Find each parasitized red blood cell.
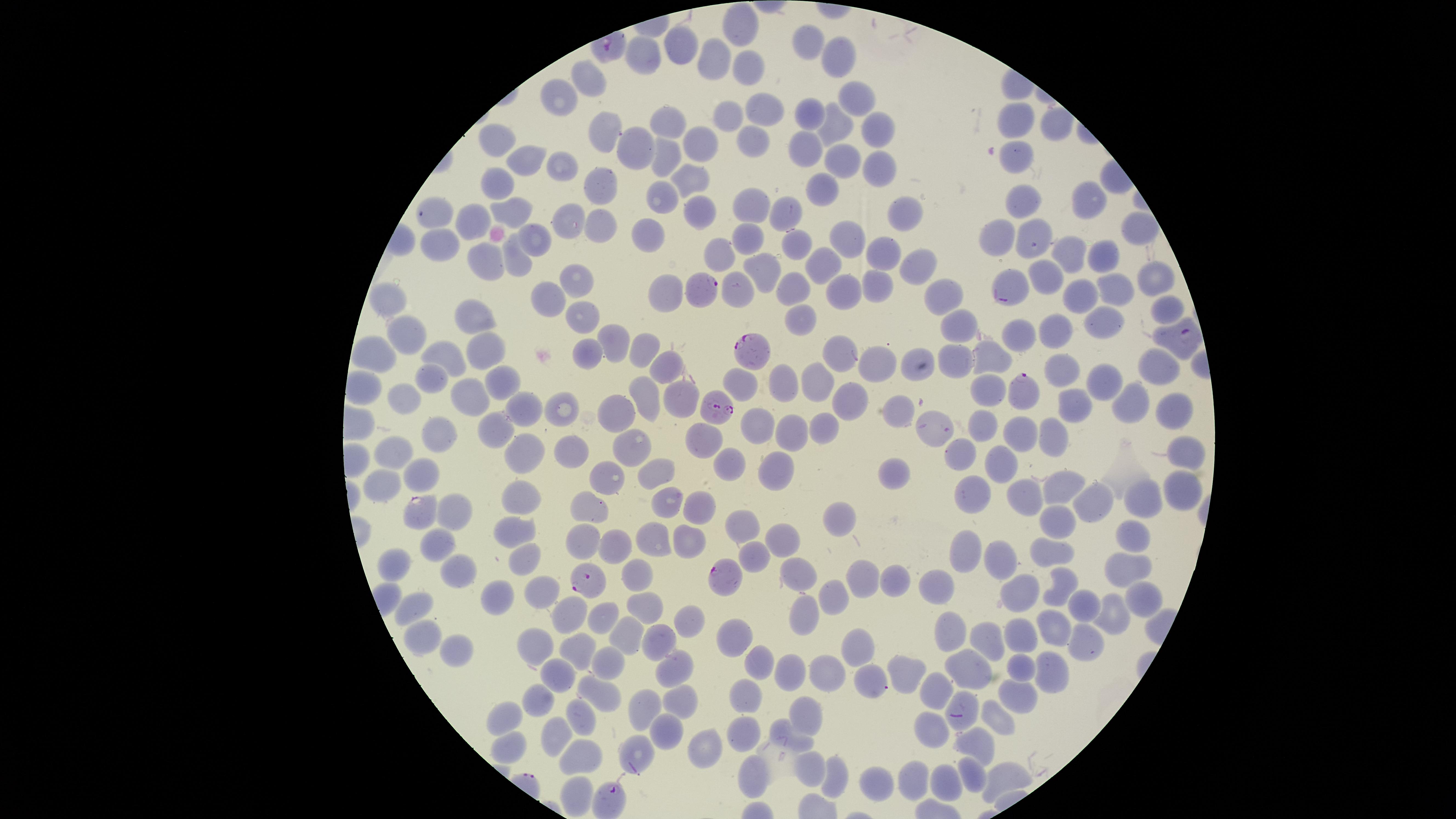
Approximate marker points, in pixels from the top-left corner.
Parasitized red blood cells: (x=705, y=288), (x=1000, y=298), (x=1184, y=336), (x=753, y=350), (x=1020, y=391), (x=717, y=406), (x=418, y=513), (x=722, y=574), (x=586, y=581), (x=955, y=712), (x=612, y=799).

Approximate marker points, in pixels from the top-left corner.
Summary:
  - Uninfected red blood cells: (x=739, y=28), (x=808, y=42), (x=677, y=50), (x=842, y=52), (x=642, y=58), (x=716, y=65), (x=746, y=68), (x=586, y=79), (x=556, y=96), (x=856, y=96), (x=761, y=109), (x=812, y=111), (x=725, y=118), (x=1016, y=119), (x=1057, y=124), (x=669, y=125), (x=834, y=126), (x=877, y=131), (x=607, y=132), (x=497, y=139), (x=705, y=141), (x=749, y=143), (x=806, y=147), (x=634, y=148), (x=1016, y=154), (x=526, y=157), (x=665, y=157), (x=843, y=158), (x=881, y=165), (x=560, y=167), (x=687, y=174), (x=499, y=184), (x=601, y=188), (x=824, y=190), (x=1084, y=197), (x=1026, y=201), (x=662, y=202), (x=697, y=206), (x=749, y=206), (x=509, y=210), (x=786, y=212), (x=433, y=213), (x=901, y=213), (x=564, y=218), (x=594, y=223), (x=471, y=225), (x=1138, y=225), (x=653, y=235), (x=1043, y=235), (x=532, y=236), (x=846, y=238), (x=748, y=240), (x=1001, y=242), (x=791, y=243), (x=441, y=246), (x=719, y=251), (x=880, y=253), (x=1071, y=253), (x=1101, y=258), (x=481, y=261), (x=911, y=261), (x=823, y=263), (x=515, y=264), (x=765, y=266), (x=1043, y=273), (x=1158, y=273), (x=578, y=280), (x=875, y=280), (x=793, y=285), (x=1112, y=286), (x=843, y=287), (x=738, y=290), (x=663, y=291), (x=944, y=293), (x=555, y=295), (x=1082, y=295), (x=380, y=303), (x=1164, y=310), (x=581, y=314), (x=803, y=314), (x=479, y=317), (x=1103, y=318), (x=962, y=326), (x=1049, y=331), (x=410, y=333), (x=1015, y=333), (x=615, y=334), (x=373, y=344), (x=484, y=349), (x=589, y=349), (x=639, y=349), (x=834, y=355), (x=957, y=356), (x=453, y=357), (x=871, y=359), (x=997, y=360), (x=663, y=367), (x=1066, y=367), (x=908, y=368), (x=1153, y=368), (x=1099, y=376), (x=433, y=377), (x=811, y=379), (x=503, y=380), (x=742, y=380), (x=784, y=382), (x=367, y=384), (x=995, y=384), (x=645, y=393), (x=683, y=395), (x=470, y=396), (x=854, y=398), (x=404, y=401), (x=1139, y=402), (x=529, y=405), (x=1177, y=406), (x=556, y=407), (x=1077, y=408), (x=901, y=411), (x=617, y=414), (x=980, y=422), (x=756, y=424), (x=831, y=424), (x=499, y=428), (x=792, y=431), (x=931, y=432), (x=439, y=434), (x=1054, y=434), (x=1018, y=436), (x=700, y=440), (x=1188, y=449), (x=633, y=451), (x=531, y=452), (x=392, y=453), (x=575, y=453), (x=956, y=458), (x=1002, y=462), (x=727, y=467), (x=779, y=469), (x=655, y=471), (x=893, y=471), (x=419, y=474), (x=604, y=476), (x=381, y=482), (x=1061, y=489), (x=976, y=491), (x=1181, y=493), (x=517, y=494), (x=1094, y=498), (x=1024, y=499), (x=669, y=500), (x=1146, y=500), (x=704, y=502), (x=588, y=511), (x=453, y=513), (x=837, y=517), (x=742, y=518), (x=1054, y=525), (x=517, y=528), (x=1126, y=535), (x=655, y=536), (x=579, y=537), (x=781, y=539), (x=690, y=542), (x=433, y=543), (x=614, y=551), (x=1055, y=554), (x=755, y=555), (x=959, y=556), (x=996, y=557), (x=525, y=558), (x=397, y=566), (x=462, y=566), (x=1122, y=571), (x=897, y=575), (x=643, y=577), (x=794, y=577), (x=857, y=577), (x=1061, y=585), (x=938, y=586), (x=540, y=587), (x=830, y=591), (x=1017, y=592), (x=1138, y=594), (x=494, y=596), (x=1088, y=603), (x=418, y=606), (x=651, y=607), (x=565, y=614), (x=801, y=614), (x=1107, y=616), (x=690, y=618), (x=600, y=619), (x=1059, y=626), (x=954, y=634), (x=625, y=635), (x=732, y=636), (x=420, y=637), (x=985, y=637), (x=1021, y=638), (x=1085, y=639), (x=856, y=641), (x=655, y=644), (x=533, y=646), (x=456, y=649), (x=578, y=651), (x=608, y=661), (x=1020, y=663), (x=764, y=664), (x=674, y=665), (x=906, y=671), (x=959, y=671), (x=824, y=672), (x=1052, y=672), (x=788, y=673), (x=882, y=679), (x=566, y=680), (x=936, y=690), (x=1022, y=695), (x=603, y=697), (x=750, y=698), (x=540, y=699), (x=677, y=701), (x=811, y=707), (x=643, y=709), (x=586, y=711), (x=997, y=715), (x=506, y=719), (x=932, y=728), (x=560, y=731), (x=663, y=732), (x=749, y=734), (x=797, y=734), (x=705, y=742), (x=505, y=745), (x=977, y=747), (x=583, y=752), (x=629, y=752), (x=810, y=764), (x=751, y=769), (x=971, y=771), (x=834, y=779), (x=881, y=779), (x=1003, y=779), (x=913, y=781), (x=950, y=783), (x=576, y=792)
  - Preparation: thin blood smear
  - Stain: Giemsa
  - Species: Plasmodium falciparum
  - Capture: smartphone photograph through the microscope eyepiece
  - Visible region: circular
  - Image size: 1456×819 pixels
  - Field of view: single